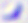
modality = photomicrograph
magnification = 400x
identification = Toxoplasma gondii